Name the blood parasite species.
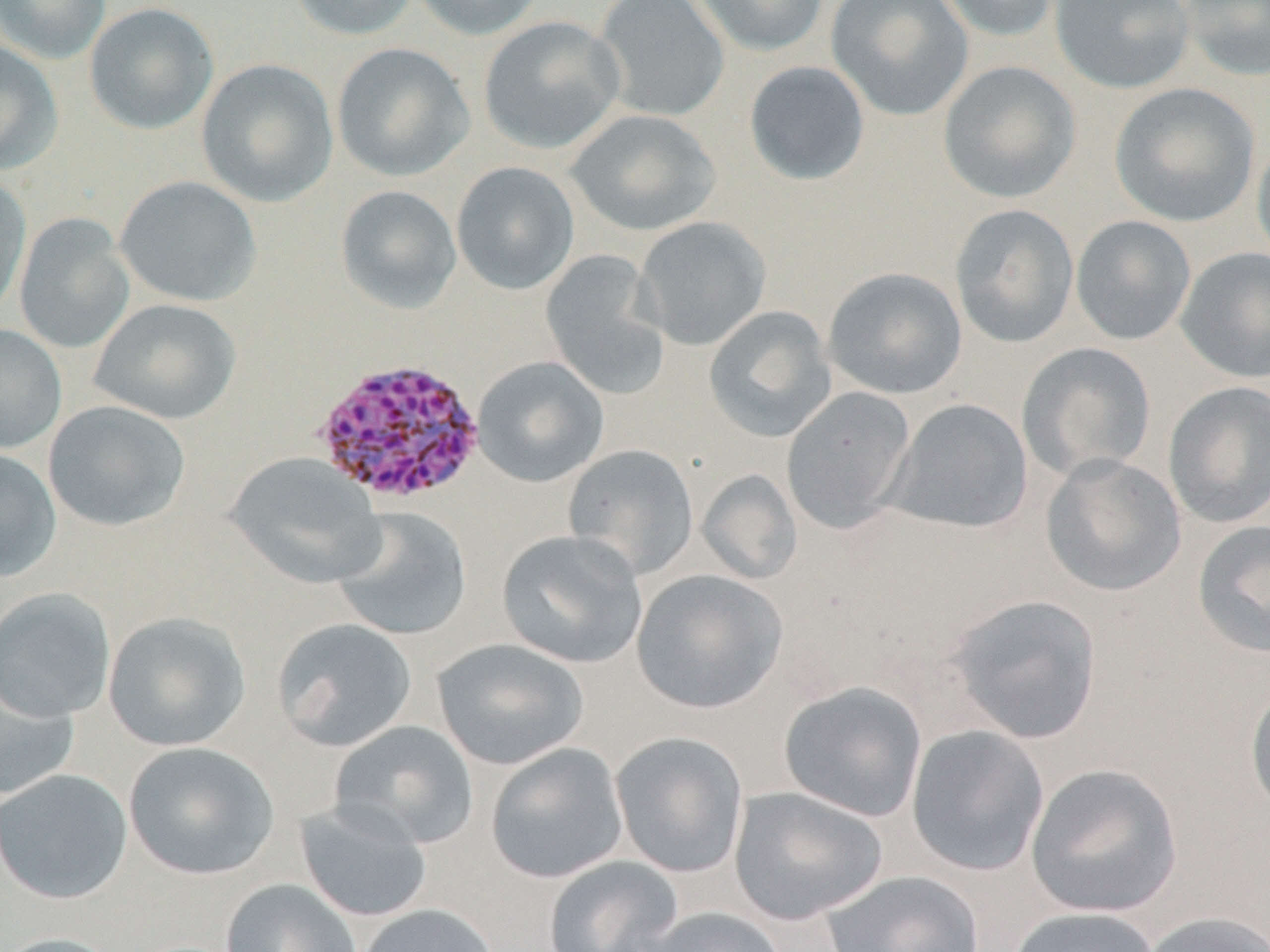
Plasmodium vivax.

stain = May-Grünwald-Giemsa
magnification = 1000x
image size = 1270×952 pixels
preparation = thin blood smear
field of view = one of a larger specimen
modality = light microscopy
uninfected red blood cell locations = approximate bounding boxes as (x1,y1)-(x2,y2) corner pairs in pixels: (0,0)-(111,65), (287,0)-(420,40), (408,0)-(546,41), (594,0)-(729,122), (690,0)-(831,57), (826,0)-(974,121), (933,0)-(1063,42), (1049,0)-(1196,94), (1178,0)-(1270,81), (84,2)-(219,135), (477,15)-(626,155), (0,40)-(64,175), (331,42)-(474,182), (196,58)-(338,207), (937,60)-(1082,204), (744,61)-(870,186), (1109,82)-(1260,227), (565,109)-(721,237), (1251,132)-(1270,270), (450,161)-(580,295), (0,173)-(32,320), (114,175)-(261,307), (335,184)-(462,315), (949,203)-(1079,348), (14,212)-(135,354), (1070,215)-(1196,346), (633,216)-(771,350), (1176,247)-(1270,383), (540,249)-(672,400), (822,267)-(967,400), (88,298)-(242,425), (703,305)-(836,443), (0,324)-(66,455), (1017,341)-(1156,482), (472,356)-(609,487), (1163,381)-(1270,529), (781,387)-(917,533), (885,398)-(1033,534), (43,400)-(191,531), (562,444)-(699,580), (0,447)-(62,583), (225,451)-(384,589), (1040,453)-(1186,597), (696,469)-(802,585), (331,506)-(472,641), (1191,518)-(1270,660), (496,529)-(648,669), (631,569)-(787,714), (0,587)-(116,722), (944,594)-(1102,744), (103,611)-(251,752), (271,618)-(418,753), (432,638)-(589,770), (0,665)-(80,800), (1244,680)-(1270,822), (779,681)-(927,822), (329,720)-(479,848), (906,725)-(1049,877), (610,731)-(749,878), (123,741)-(280,880), (485,742)-(630,883), (1025,763)-(1183,918), (0,769)-(133,904), (728,786)-(887,924), (294,800)-(433,922), (542,855)-(684,952), (820,869)-(984,952), (220,878)-(362,952), (354,903)-(499,952), (634,905)-(788,952), (1006,906)-(1161,952), (1138,910)-(1270,952), (0,932)-(125,952)
Plasmodium vivax-infected red blood cell locations = approximate bounding boxes as (x1,y1)-(x2,y2) corner pairs in pixels: (311,357)-(486,507)